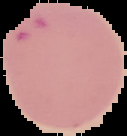

Summary:
  - Preparation: thin blood smear
  - Malaria status: parasitized
  - Image size: 127×136 pixels
  - Image type: segmented cell region on a black background